Report the malaria status of this cell.
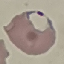

It is parasitized.

capture = smartphone camera at the microscope eyepiece
stain = Giemsa
image type = cell patch, automatically extracted from a larger field of view and resized to 64 × 64 pixels
preparation = thin smear